State which parasite is depicted.
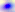

This is Toxoplasma gondii.

Captured at 400x magnification. Photomicrograph.